Report the malaria status of this cell.
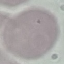
Uninfected.

Summary:
  - Capture: smartphone through the microscope eyepiece
  - Stain: Giemsa
  - Preparation: thin smear
  - Image type: automatically extracted cell patch, resized to 64 × 64 pixels